Classify this cell by malaria status.
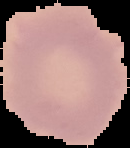

It is uninfected.

Cell region segmented out of the field of view; the surrounding area is masked to black. Image is 130×148 pixels. From a thin blood smear.